Locate every leukocyte (white blood cell).
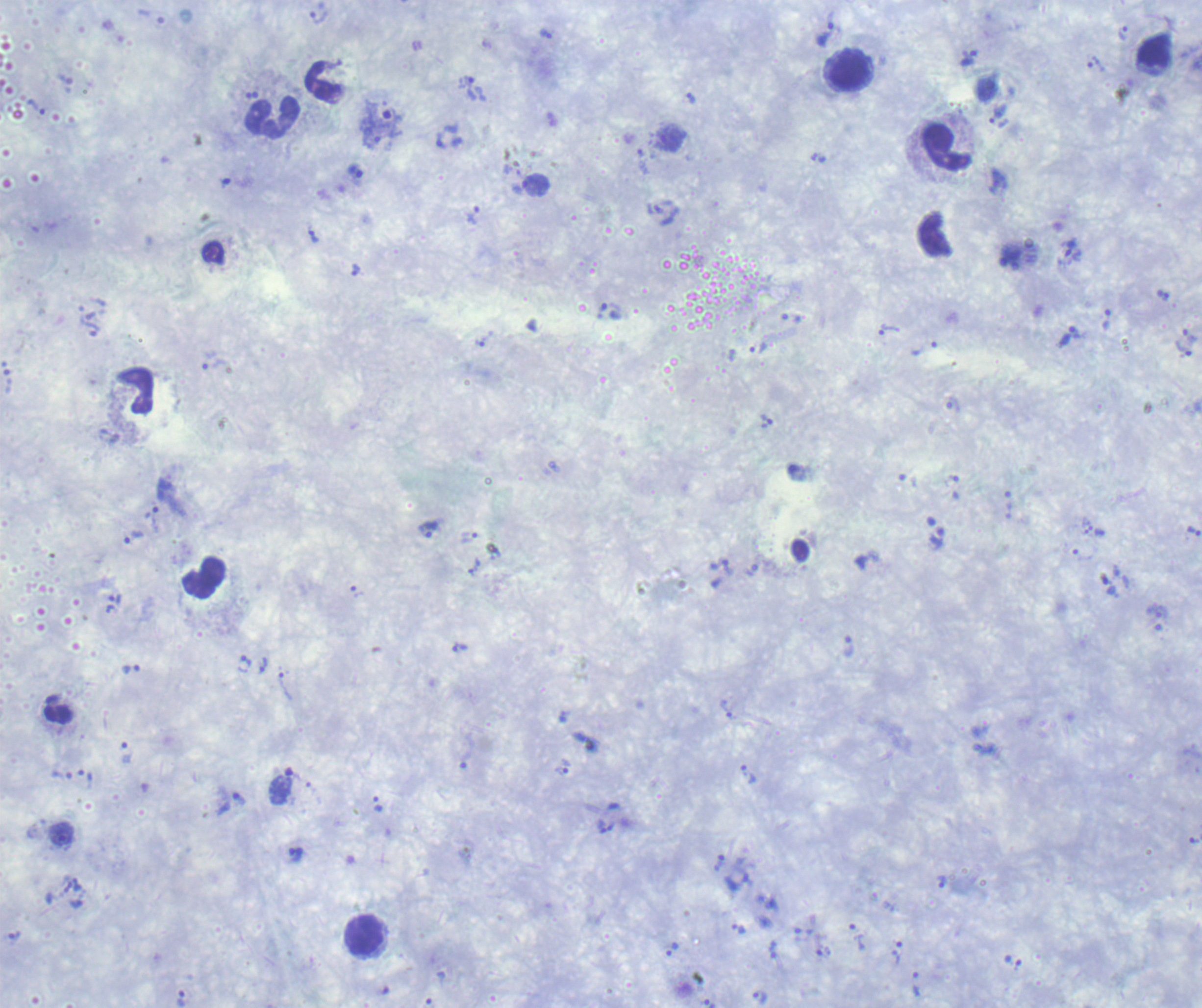

Approximate centers as {x, y} in pixels.
Leukocytes: {848, 71}, {272, 119}, {947, 148}, {204, 578}, {58, 710}, {364, 935}.

Approximate centers as {x, y} in pixels.
Summary:
  - Trophozoite locations: {1123, 34}, {825, 35}, {967, 59}, {1096, 64}, {469, 88}, {690, 99}, {998, 113}, {383, 114}, {442, 142}, {355, 172}, {473, 214}, {313, 237}, {356, 271}, {1163, 296}, {611, 310}, {887, 329}, {1071, 336}, {1190, 336}, {484, 339}, {759, 349}, {1185, 349}, {766, 422}, {153, 518}, {429, 530}, {1194, 531}, {134, 537}, {937, 538}, {474, 568}, {848, 646}, {459, 648}, {243, 663}, {262, 665}, {285, 687}, {563, 768}, {748, 775}, {282, 785}, {238, 798}, {378, 804}, {62, 834}, {296, 854}, {941, 881}, {738, 928}, {857, 937}, {673, 949}, {774, 950}, {897, 953}, {916, 984}, {759, 995}
  - Magnification: 100x
  - Background quality: unsatisfactory
  - Preparation: thick smear of blood
  - Context: previously used in a real diagnosis
  - Stain: Romanowsky
  - Image size: 1202×1008 pixels
  - Result: positive for malaria parasites
  - Field of view: single